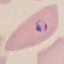

result = malaria parasites detected
image type = cell patch, automatically extracted from a larger field of view and resized to 64 × 64 pixels
capture = smartphone through the microscope eyepiece
stain = Giemsa
preparation = thin smear